Name the parasite shown.
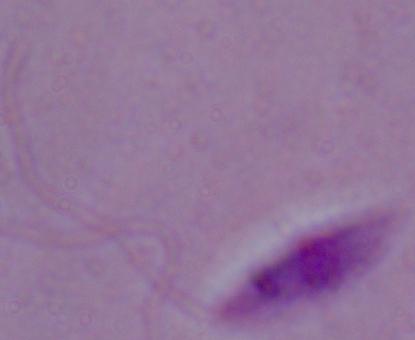

This is Leishmania.

modality = micrograph
magnification = 1000x